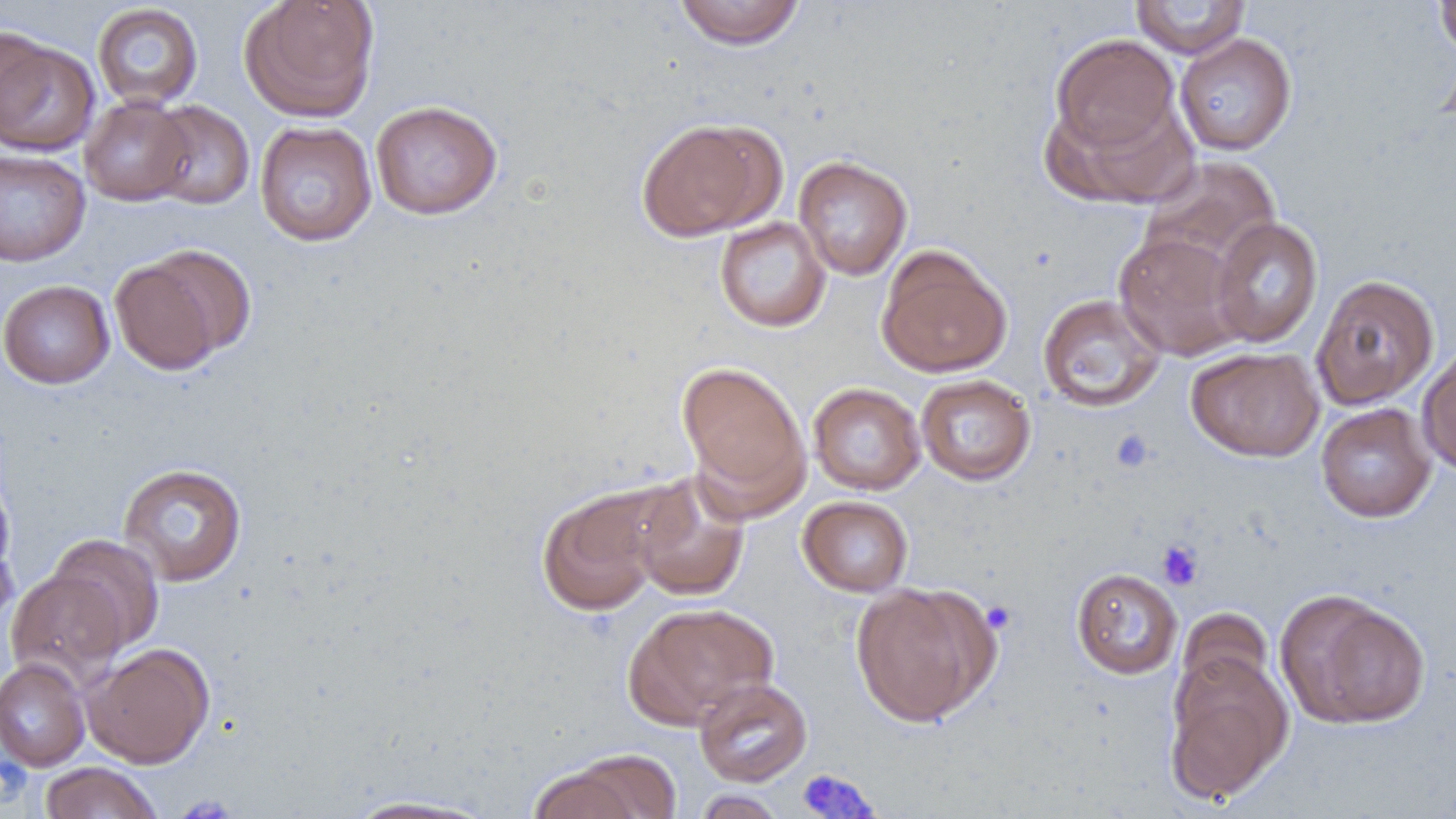 Approximate bounding boxes as (x1, y1, x2, y2) in pixels. Uninfected red blood cell locations: (241, 0, 380, 122), (673, 0, 806, 50), (1130, 0, 1251, 59), (1432, 0, 1456, 60), (92, 3, 204, 110), (1, 24, 56, 139), (1049, 32, 1183, 158), (1174, 32, 1298, 157), (0, 36, 100, 156), (1045, 94, 1194, 209), (80, 96, 194, 206), (144, 100, 256, 210), (370, 100, 503, 220), (636, 118, 780, 241), (255, 121, 377, 247), (0, 149, 91, 267), (793, 155, 912, 280), (1139, 156, 1282, 273), (714, 216, 831, 332), (1209, 217, 1324, 348), (1113, 232, 1248, 361), (875, 246, 1013, 378), (109, 248, 247, 374), (1311, 273, 1440, 410), (0, 279, 115, 388), (1038, 293, 1166, 412), (1417, 344, 1456, 476), (1185, 346, 1324, 463), (676, 361, 810, 508), (915, 374, 1036, 486), (808, 382, 926, 495), (1316, 402, 1436, 522), (117, 463, 247, 587), (0, 472, 16, 588), (629, 472, 751, 603), (535, 485, 671, 618), (798, 495, 913, 597), (0, 529, 19, 634), (47, 534, 165, 655), (1071, 567, 1183, 679), (6, 569, 126, 688), (851, 582, 995, 727), (1275, 591, 1431, 730), (624, 602, 779, 728), (1177, 606, 1274, 701), (84, 642, 215, 768), (1164, 651, 1293, 805), (0, 658, 90, 771), (694, 677, 812, 787), (527, 760, 652, 819), (39, 761, 163, 819), (692, 790, 787, 818), (340, 794, 500, 818). Platelet locations: (1111, 429, 1156, 473), (1156, 539, 1204, 590), (981, 601, 1016, 633), (0, 754, 32, 802), (795, 768, 881, 818), (173, 795, 239, 819). Slide-level diagnosis: no evidence of blood parasites. Thin blood film. Light microscopy. Captured at 1000x magnification. Single field of view. Image is 1456×819 pixels.